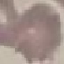
Result: no malaria parasites seen. Giemsa-stained preparation. Automatically extracted cell patch, resized to 64 × 64 pixels. Photographed with a smartphone camera at the microscope eyepiece. Thin blood smear.